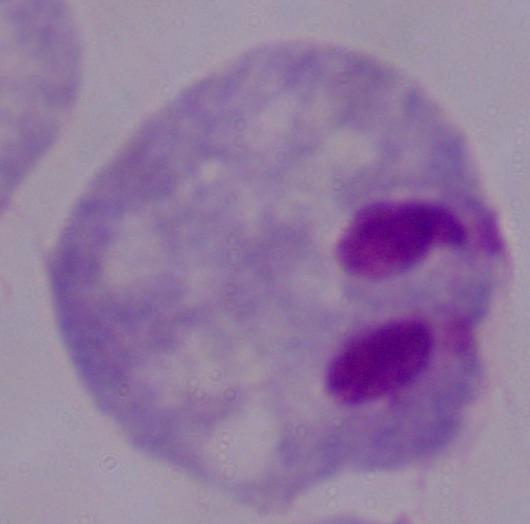

Photomicrograph. Captured at 1000x magnification. A trichomonad is seen.